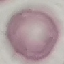
result = no malaria parasites seen
stain = Giemsa
image type = cell patch, automatically extracted from a larger field of view and resized to 64 × 64 pixels
capture = smartphone through the microscope eyepiece
preparation = thin blood smear